Locate every malaria parasite.
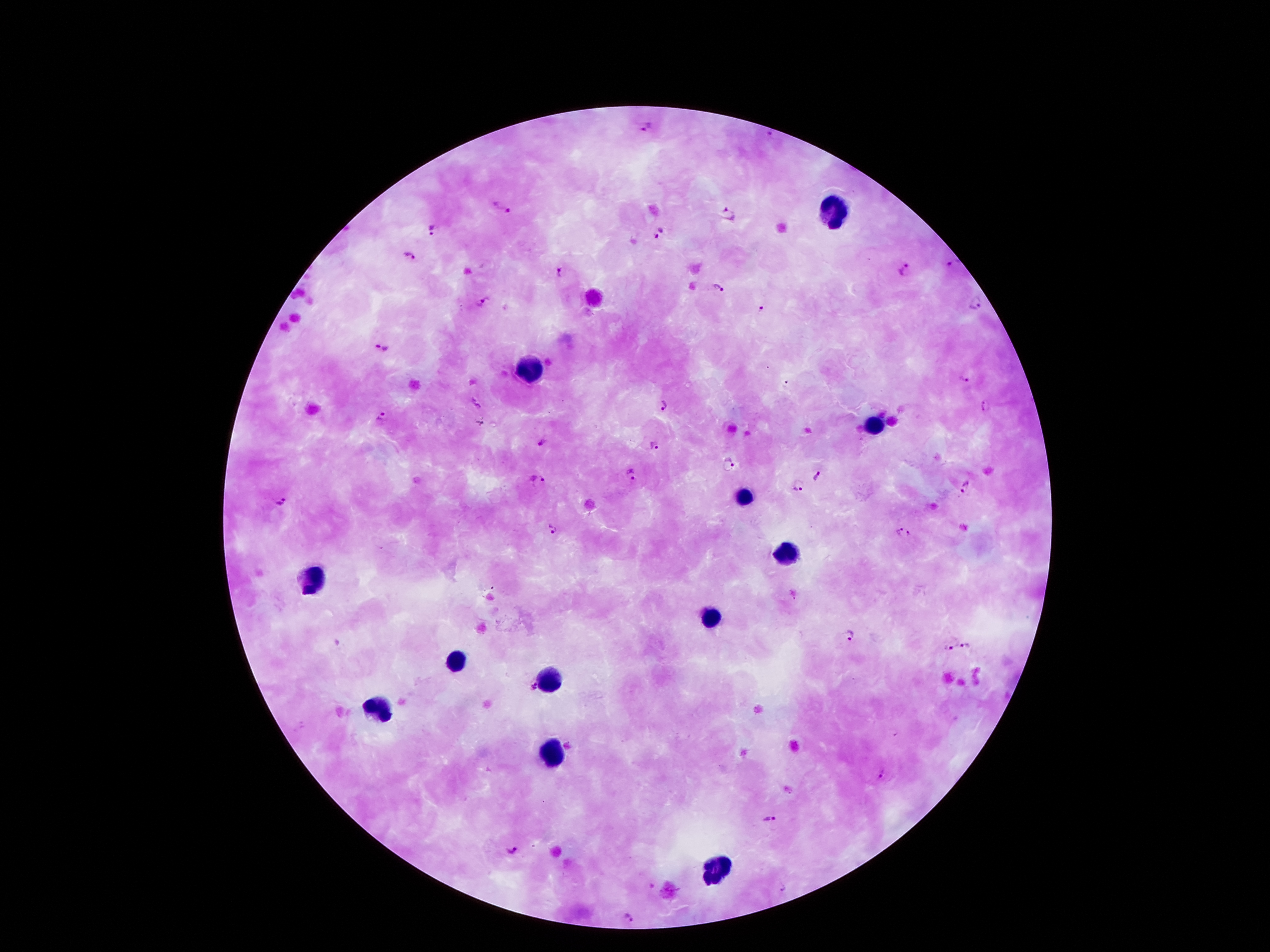

Approximate centers as {x, y} in pixels.
Malaria parasites: {648, 126}, {773, 133}, {502, 210}, {728, 215}, {435, 232}, {659, 236}, {410, 257}, {954, 264}, {906, 270}, {558, 272}, {718, 287}, {484, 302}, {977, 305}, {764, 311}, {383, 346}, {964, 380}, {787, 385}, {663, 404}, {477, 405}, {986, 408}, {383, 416}, {482, 423}, {542, 442}, {653, 446}, {731, 465}, {632, 476}, {819, 476}, {538, 481}, {799, 487}, {967, 487}, {281, 501}, {553, 529}, {898, 532}, {910, 533}, {849, 637}, {969, 646}, {948, 648}, {530, 688}, {881, 774}, {768, 820}, {512, 851}, {782, 888}, {627, 918}.

leukocyte locations = {833, 218}, {528, 368}, {876, 425}, {746, 498}, {787, 555}, {310, 580}, {708, 616}, {456, 661}, {549, 682}, {378, 709}, {555, 754}, {717, 873}
stain = Giemsa
patient malaria status = positive for Plasmodium falciparum
capture = smartphone through the microscope eyepiece
field of view = single
image size = 1270×952 pixels
magnification = 100x
preparation = thick peripheral-blood smear